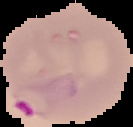
preparation: thin blood smear
image_type: cell region segmented out of the field of view; surrounding area masked to black
malaria_status: parasitized
image_size: 133×127 pixels